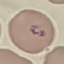

Summary:
  - Result: malaria parasites identified
  - Capture: smartphone through the microscope eyepiece
  - Stain: Giemsa
  - Image type: cell patch, automatically extracted from a larger field of view and resized to 64 × 64 pixels
  - Preparation: thin blood film